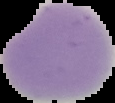

Summary:
  - Malaria status: uninfected
  - Image type: segmented cell region with the area outside set to black
  - Image size: 115×103 pixels
  - Preparation: thin blood film